Give the extent of all uninfected red blood cells.
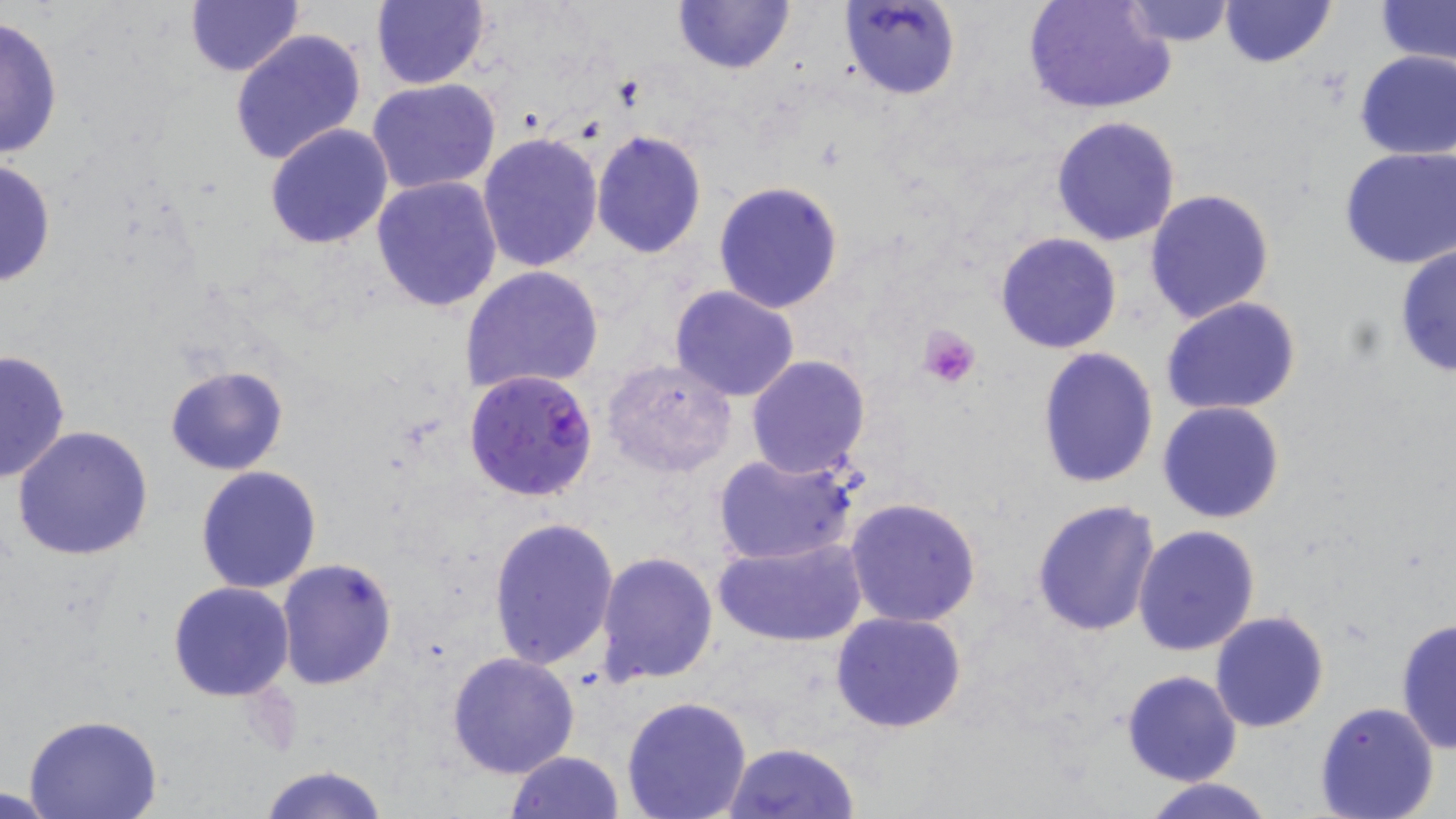

Approximate bounding boxes as named x1/y1/x2/y2 corners in pixels.
Uninfected red blood cells: (x1=370, y1=0, x2=490, y2=90), (x1=671, y1=0, x2=797, y2=76), (x1=839, y1=0, x2=960, y2=101), (x1=1022, y1=0, x2=1175, y2=117), (x1=185, y1=1, x2=304, y2=78), (x1=1120, y1=1, x2=1239, y2=47), (x1=1219, y1=1, x2=1336, y2=68), (x1=1373, y1=2, x2=1456, y2=67), (x1=0, y1=14, x2=65, y2=163), (x1=230, y1=28, x2=367, y2=165), (x1=1353, y1=49, x2=1456, y2=160), (x1=367, y1=79, x2=502, y2=196), (x1=1051, y1=114, x2=1181, y2=247), (x1=264, y1=122, x2=394, y2=249), (x1=590, y1=129, x2=708, y2=259), (x1=476, y1=132, x2=603, y2=273), (x1=1339, y1=145, x2=1456, y2=269), (x1=0, y1=157, x2=57, y2=289), (x1=371, y1=176, x2=503, y2=312), (x1=713, y1=180, x2=844, y2=315), (x1=1143, y1=188, x2=1276, y2=325), (x1=995, y1=231, x2=1123, y2=354), (x1=1394, y1=243, x2=1455, y2=378), (x1=460, y1=265, x2=604, y2=396), (x1=669, y1=285, x2=802, y2=402), (x1=1160, y1=297, x2=1303, y2=419), (x1=1036, y1=346, x2=1159, y2=489), (x1=0, y1=347, x2=70, y2=484), (x1=746, y1=355, x2=873, y2=479), (x1=601, y1=359, x2=738, y2=478), (x1=164, y1=364, x2=289, y2=476), (x1=1158, y1=401, x2=1286, y2=524), (x1=11, y1=424, x2=155, y2=561), (x1=712, y1=451, x2=858, y2=566), (x1=195, y1=465, x2=323, y2=594), (x1=844, y1=496, x2=985, y2=629), (x1=1031, y1=498, x2=1162, y2=638), (x1=488, y1=516, x2=620, y2=669), (x1=1132, y1=524, x2=1260, y2=656), (x1=713, y1=534, x2=868, y2=649), (x1=594, y1=552, x2=719, y2=687), (x1=276, y1=558, x2=399, y2=690), (x1=168, y1=581, x2=295, y2=700), (x1=832, y1=610, x2=966, y2=733), (x1=1208, y1=610, x2=1329, y2=732), (x1=1394, y1=618, x2=1455, y2=754), (x1=446, y1=652, x2=580, y2=778), (x1=1122, y1=671, x2=1243, y2=786), (x1=620, y1=697, x2=753, y2=818), (x1=1313, y1=701, x2=1441, y2=819), (x1=25, y1=715, x2=164, y2=819), (x1=723, y1=742, x2=859, y2=818), (x1=506, y1=750, x2=624, y2=819), (x1=258, y1=765, x2=390, y2=819), (x1=1141, y1=777, x2=1278, y2=819), (x1=0, y1=785, x2=66, y2=819).

Plasmodium falciparum-infected red blood cell locations = approximate bounding boxes as named x1/y1/x2/y2 corners in pixels: (x1=464, y1=370, x2=600, y2=502)
slide-level diagnosis = Plasmodium falciparum
field of view = one of a larger specimen
image size = 1456×819 pixels
preparation = thin blood film
platelet locations = approximate bounding boxes as named x1/y1/x2/y2 corners in pixels: (x1=918, y1=326, x2=982, y2=389)
magnification = 1000x
stain = May-Grünwald-Giemsa
modality = light microscopy